Assess the morphology of the red blood cells.
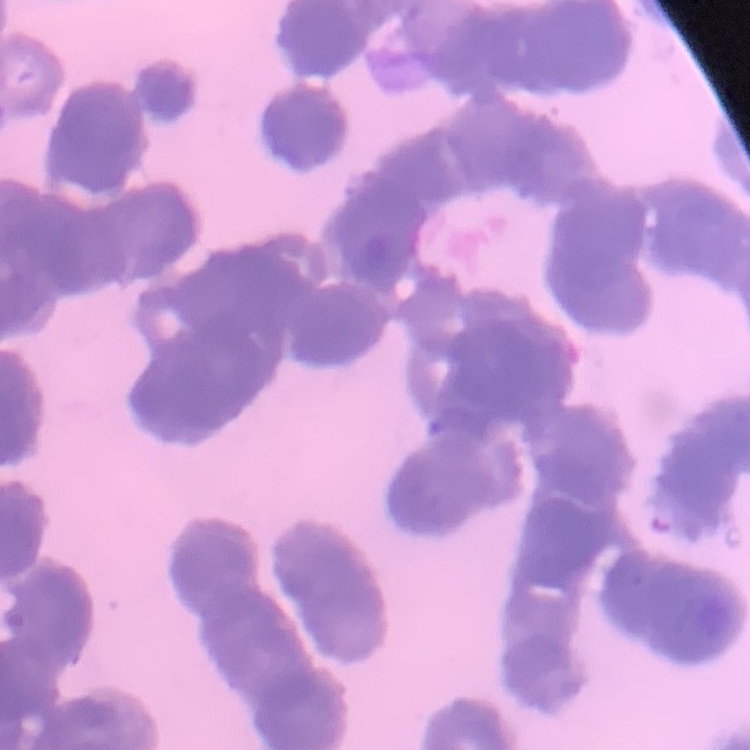
They show rouleaux formation.

Thin peripheral smear. One tile cut from a larger photomicrograph. Field's or Giemsa stain.